State which parasite is depicted.
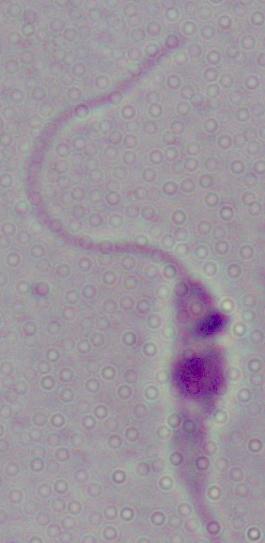
This is Leishmania.

Summary:
  - Magnification: 1000x
  - Modality: micrograph